Name the parasite shown.
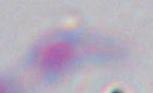

This is Toxoplasma gondii.

modality: micrograph
magnification: 1000x